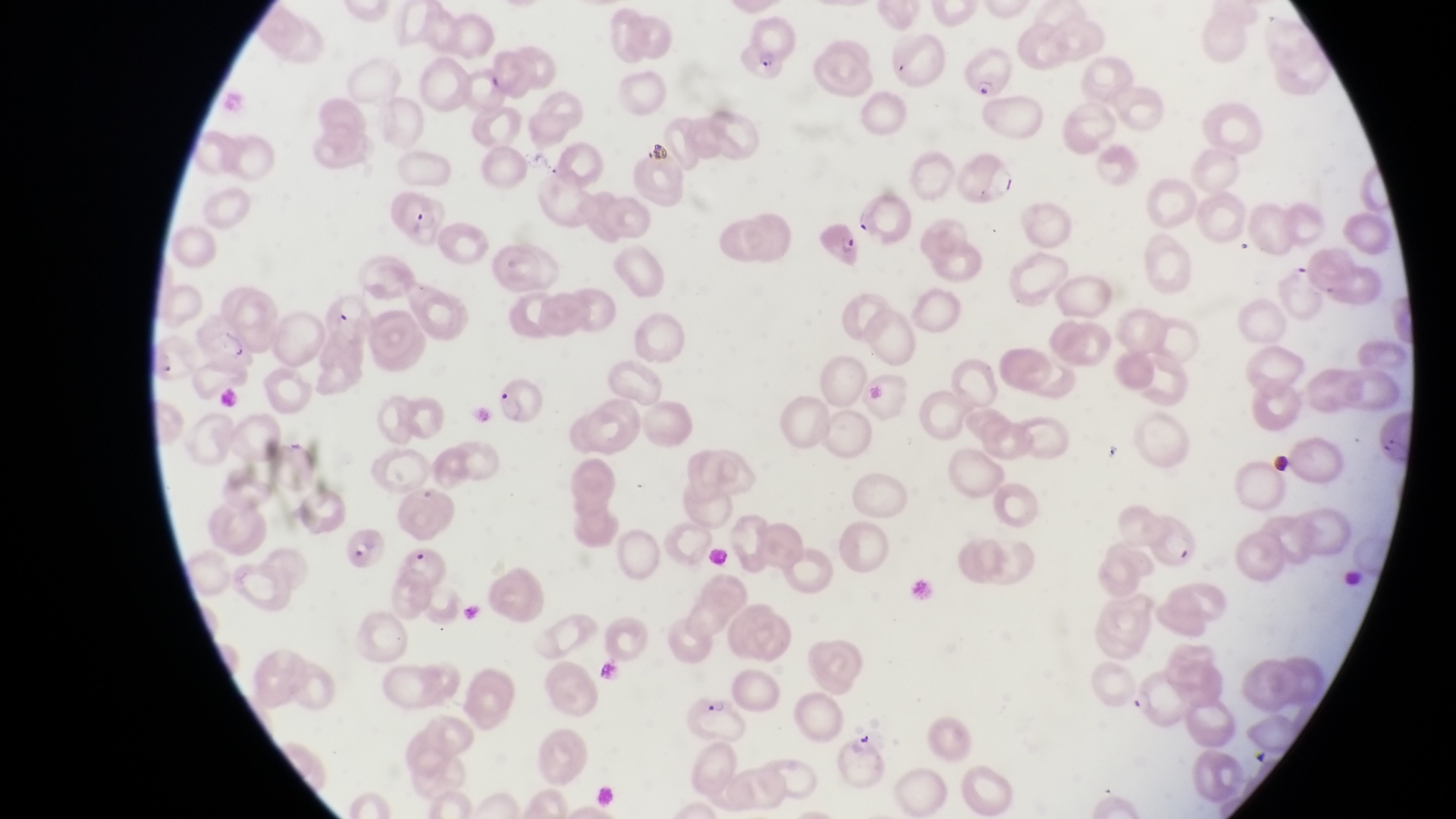

Approximate bounding boxes as {left, top, right, bottom} in pixels. Parasitised red blood cell locations: {745, 14, 797, 78}, {962, 49, 1017, 105}, {952, 151, 1016, 207}, {391, 191, 444, 250}, {812, 217, 868, 269}, {323, 288, 366, 337}, {193, 323, 254, 381}, {491, 380, 543, 426}, {1366, 415, 1413, 470}, {1140, 513, 1197, 572}, {343, 519, 389, 571}, {397, 548, 452, 594}, {1131, 674, 1197, 733}, {690, 695, 753, 738}. Artifact (platelet-like body, stain precipitate, or debris) locations: {644, 139, 674, 168}, {1266, 450, 1293, 479}. Photographed through the eyepiece of an Olympus CX-23 microscope with a smartphone camera. Magnification of 1000x. Thin blood film. Image is 1456×819 pixels. Collected in Uganda. One field of view.